Identify the parasite.
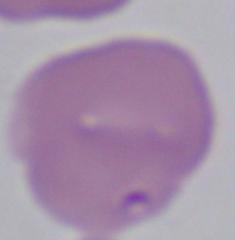
Babesia.

Summary:
  - Modality: photomicrograph
  - Magnification: 1000x